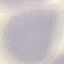
Summary:
  - Result: negative for malaria parasites
  - Image type: automatically extracted cell patch, resized to 64 × 64 pixels
  - Stain: Giemsa
  - Capture: smartphone through the microscope eyepiece
  - Preparation: thin blood smear